Give the position of every Plasmodium parasite visible.
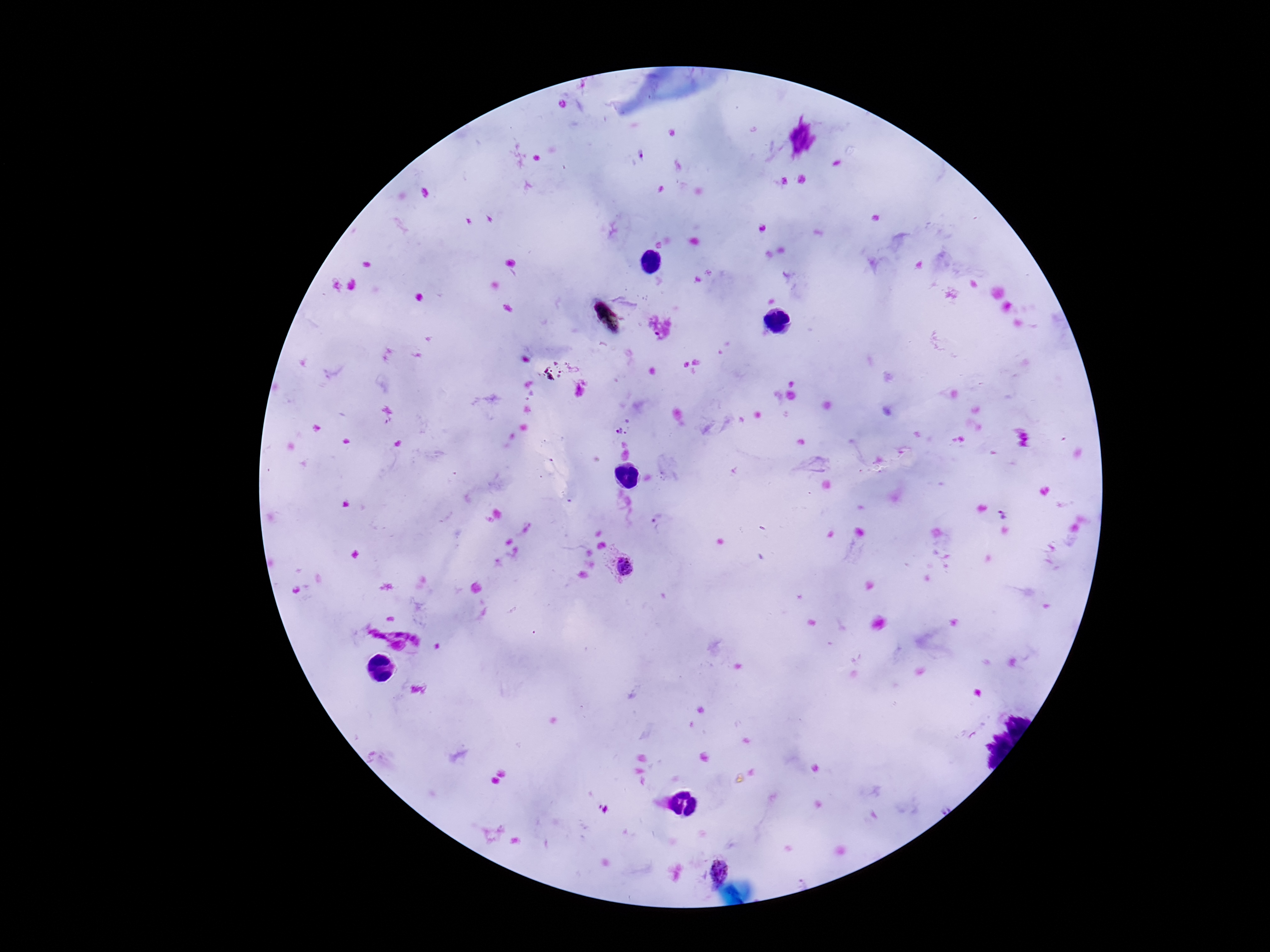
Approximate centers as (x, y) in pixels.
Plasmodium parasites: (641, 155), (617, 430), (1000, 512), (659, 521), (622, 566), (710, 870).

Giemsa stain. One field from this slide. Image is 1270×952 pixels. Thick peripheral-blood smear. Patient malaria status: infected. Photographed through the microscope eyepiece with a smartphone camera. 100x magnification.